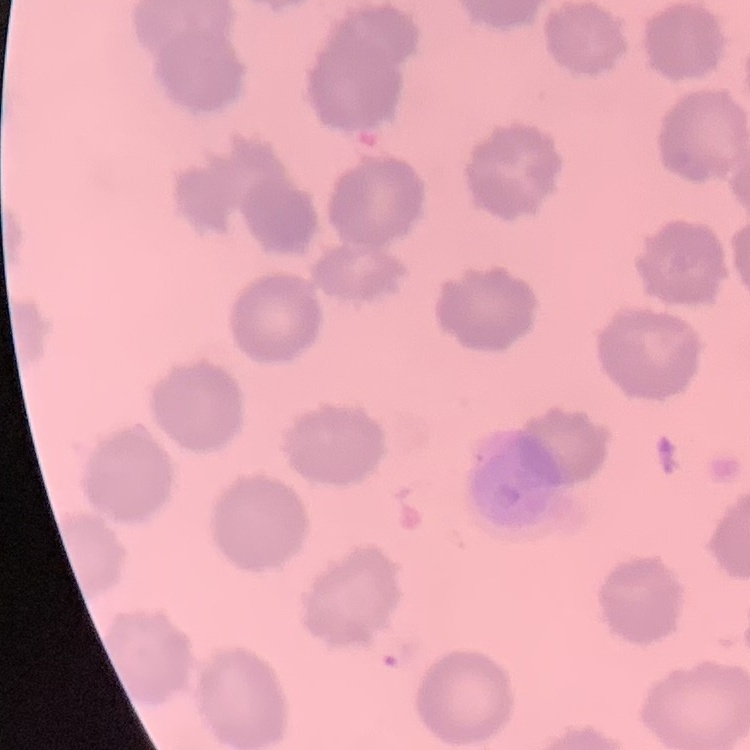
Summary:
  - Erythrocyte morphology: no rouleaux formation
  - Preparation: thin blood film
  - Stain: Field's or Giemsa
  - Image type: square crop of a larger photomicrograph